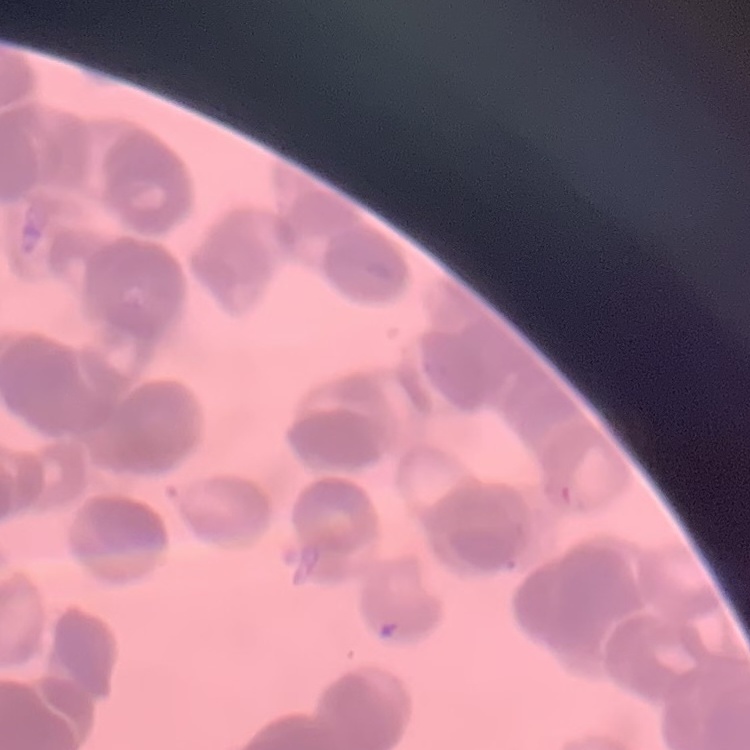
{
  "erythrocyte_morphology": "rouleaux formation",
  "image_type": "square crop of a larger photomicrograph",
  "preparation": "thin blood smear",
  "stain": "Field's or Giemsa"
}